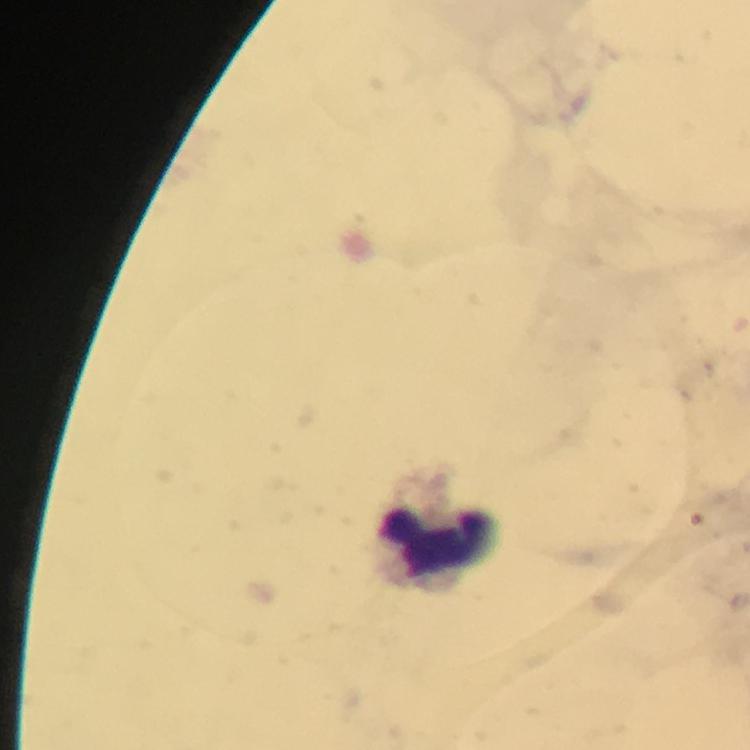
Approximate centers as [x, y] in pixels.
Summary:
  - Leukocyte locations: [443, 544]
  - Immersion oil: applied
  - Stain: Giemsa
  - Preparation: thick smear
  - Context: from a diagnostic examination for malaria
  - Capture: smartphone camera through the microscope
  - Image size: 750×750 pixels
  - Magnification: 100x
  - Malaria parasites: none detected
  - Cropped from: one field of view